Point out Plasmodium parasites and leukocytes.
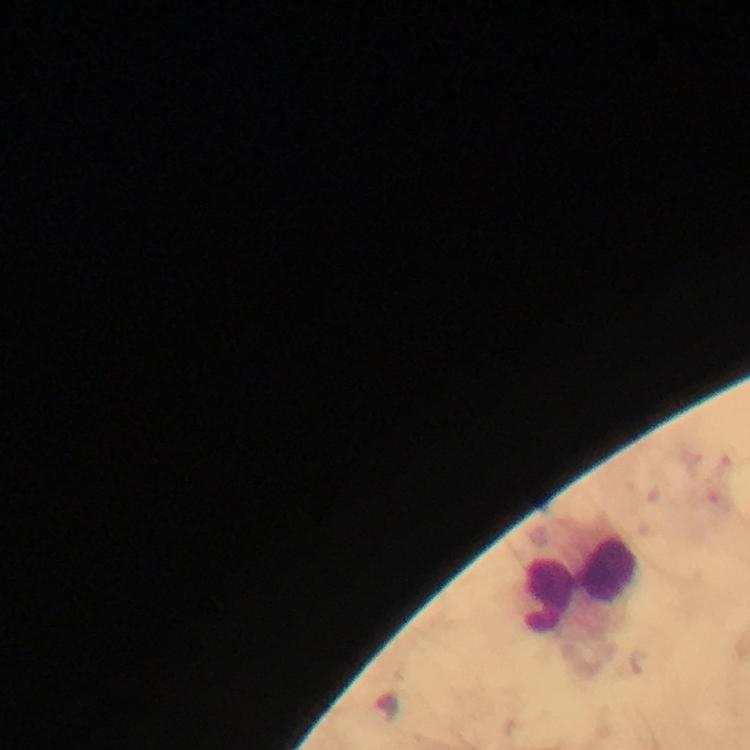

No Plasmodium parasites detected.
Approximate centers as (x, y) in pixels.
Leukocytes: (578, 586).

stain = Giemsa
image size = 750×750 pixels
magnification = 100x
capture = smartphone mounted on the microscope
context = from a diagnostic examination for malaria
cropped from = one field of view
immersion oil = used
preparation = thick blood film